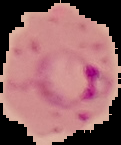

{
  "image_size": "121×145 pixels",
  "preparation": "thin blood smear",
  "image_type": "segmented cell region with the area outside set to black",
  "result": "Plasmodium parasites detected"
}